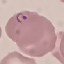 Result: malaria parasites detected. Acquired by smartphone through the microscope eyepiece. Automatically extracted cell patch, resized to 64 × 64 pixels. Thin blood film. Giemsa-stained preparation.